Locate every blood parasite and identify its species.
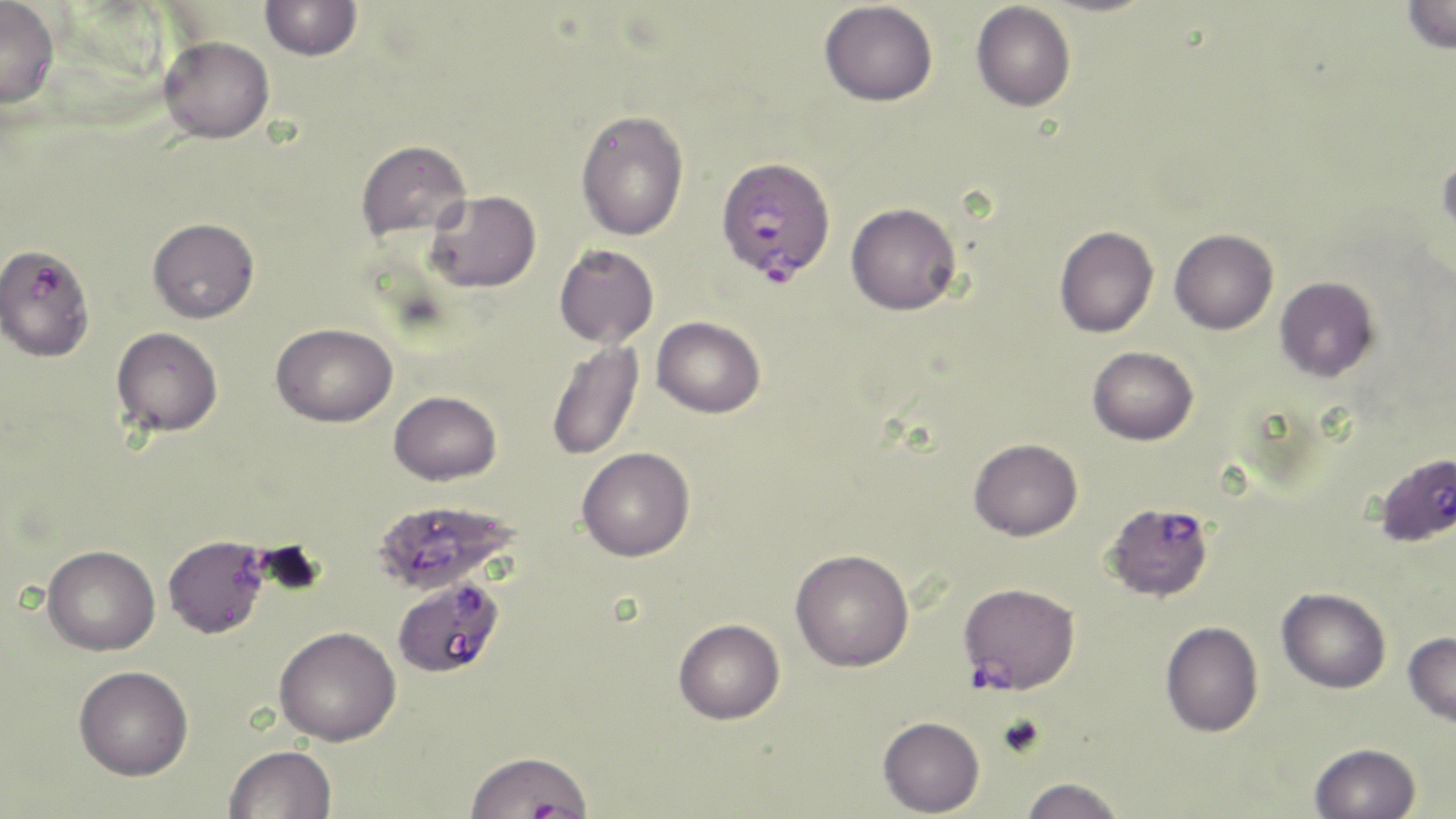
Approximate bounding boxes as (x1,y1)-(x2,y2) corner pairs in pixels.
Plasmodium falciparum-infected red blood cells: (715,156)-(835,284), (0,243)-(95,362), (1374,452)-(1456,547), (375,501)-(519,593), (1109,501)-(1211,603), (163,535)-(271,638), (393,573)-(504,678), (958,582)-(1080,694).
No Plasmodium ovale, Plasmodium malariae, Plasmodium vivax, Babesia divergens, or Trypanosoma brucei observed.

slide-level diagnosis = Plasmodium falciparum
magnification = 1000x
image size = 1456×819 pixels
uninfected red blood cell locations = approximate bounding boxes as (x1,y1)-(x2,y2) corner pairs in pixels: (1402,0)-(1456,54), (0,1)-(60,109), (259,1)-(362,61), (819,1)-(937,106), (971,2)-(1076,111), (159,36)-(274,143), (576,110)-(689,241), (355,140)-(472,241), (1437,148)-(1456,245), (424,190)-(541,293), (846,202)-(961,314), (148,217)-(259,323), (1054,225)-(1158,338), (1169,228)-(1278,334), (554,244)-(659,348), (1275,276)-(1379,382), (652,316)-(766,418), (271,323)-(397,427), (111,326)-(223,437), (546,340)-(644,462), (1087,346)-(1198,445), (389,390)-(501,485), (969,438)-(1082,540), (576,447)-(695,561), (42,544)-(160,655), (790,548)-(914,671), (1277,587)-(1391,693), (673,618)-(785,724), (1160,621)-(1263,737), (274,626)-(401,746), (1403,631)-(1456,726), (74,665)-(193,780), (878,716)-(985,816), (1310,742)-(1421,819), (224,745)-(336,819), (462,749)-(595,819), (1019,777)-(1126,819)
modality = optical microscopy
stain = May-Grünwald-Giemsa
field of view = single
preparation = thin blood smear